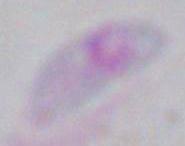

modality = photomicrograph
identification = Toxoplasma gondii
magnification = 1000x